Locate every blood parasite and identify its species.
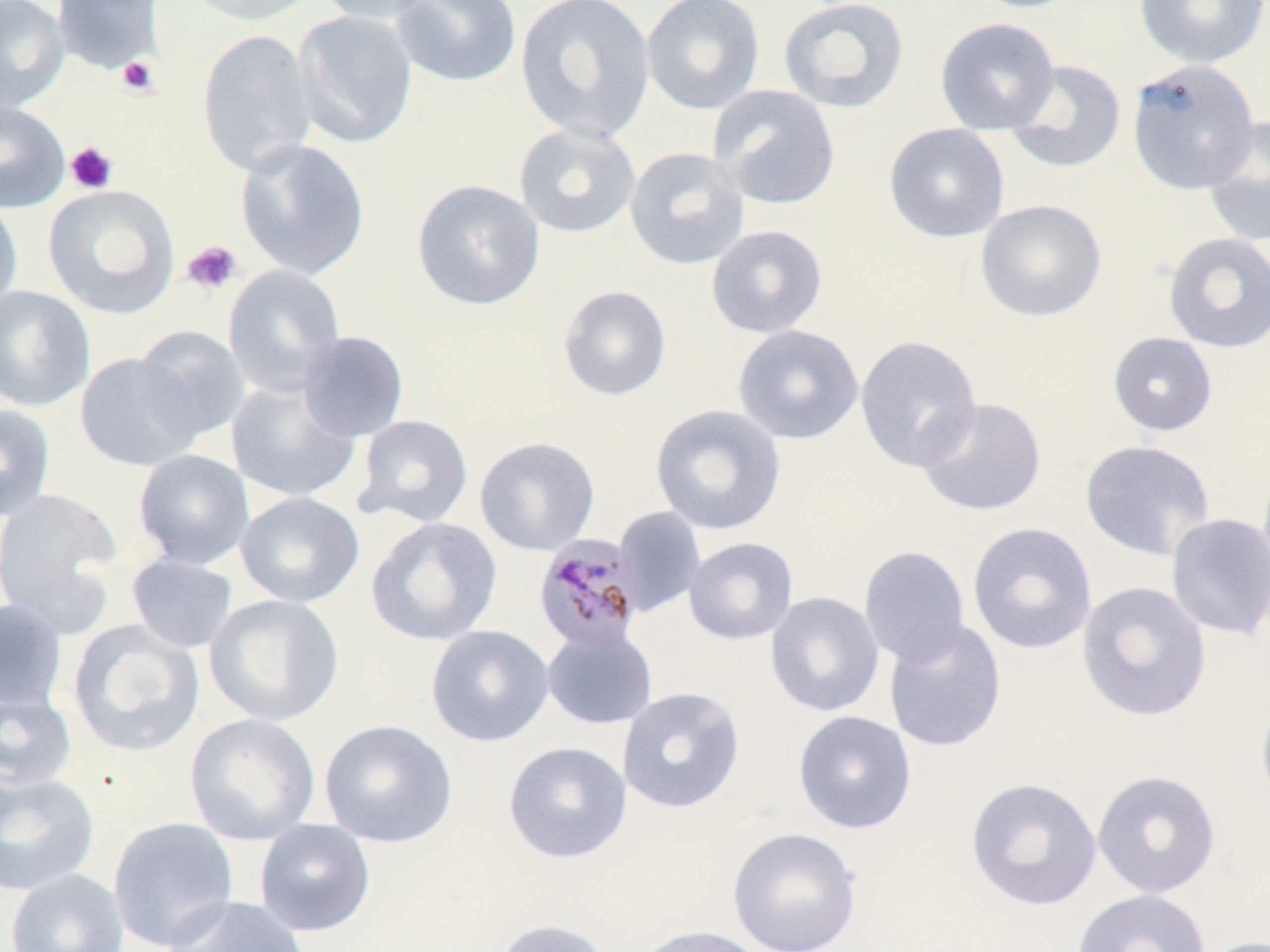

Approximate bounding boxes as (x1,y1)-(x2,y2) corner pairs in pixels.
Plasmodium malariae-infected red blood cells: (532,533)-(646,653).
No Plasmodium falciparum, Plasmodium ovale, Plasmodium vivax, Babesia divergens, or Trypanosoma brucei observed.

slide_level_diagnosis: Plasmodium malariae
modality: optical microscopy
platelet_locations: 'approximate bounding boxes as (x1,y1)-(x2,y2) corner pairs in pixels: (117,56)-(158,97), (65,142)-(118,194), (182,241)-(242,296)'
uninfected_red_blood_cell_locations: 'approximate bounding boxes as (x1,y1)-(x2,y2) corner pairs in pixels: (0,0)-(70,112), (51,0)-(162,74), (180,0)-(319,26), (316,0)-(441,25), (390,0)-(522,88), (515,0)-(657,144), (640,0)-(765,115), (1134,0)-(1269,69), (778,1)-(910,115), (292,10)-(418,149), (934,17)-(1060,135), (197,28)-(318,177), (1127,58)-(1262,195), (1003,59)-(1127,174), (708,84)-(841,210), (0,99)-(70,212), (1201,115)-(1270,247), (514,122)-(641,239), (883,123)-(1010,243), (234,138)-(371,281), (624,146)-(749,270), (411,178)-(545,311), (42,184)-(180,319), (0,197)-(23,315), (975,199)-(1107,322), (706,224)-(828,338), (1163,232)-(1270,353), (222,264)-(346,397), (0,285)-(96,412), (558,285)-(671,401), (732,324)-(864,444), (131,325)-(251,443), (296,330)-(410,442), (1108,331)-(1217,436), (854,334)-(983,472), (75,352)-(204,472), (226,378)-(361,503), (915,397)-(1047,517), (0,403)-(56,521), (650,404)-(786,535), (352,415)-(474,528), (474,437)-(600,556), (1079,439)-(1216,562), (132,449)-(255,570), (0,487)-(124,632), (235,491)-(365,608), (613,506)-(707,618), (1166,512)-(1270,641), (365,517)-(502,647), (967,522)-(1097,654), (683,537)-(798,645), (858,545)-(970,666), (126,554)-(239,653), (1077,581)-(1211,722), (765,591)-(885,717), (205,594)-(345,727), (0,599)-(69,714), (884,618)-(1006,753), (67,620)-(206,758), (425,625)-(554,747), (541,625)-(658,730), (1,685)-(78,791), (617,686)-(746,814), (1255,692)-(1270,809), (792,710)-(917,834), (184,713)-(321,846), (318,719)-(458,848), (503,741)-(632,864), (0,768)-(101,896), (1092,769)-(1222,899), (966,776)-(1102,911), (107,816)-(240,952), (253,819)-(376,937), (727,827)-(862,952), (6,868)-(130,952), (1072,889)-(1211,952), (164,896)-(311,952), (492,918)-(615,952), (632,924)-(774,952), (1198,935)-(1270,952)'
stain: May-Grünwald-Giemsa
magnification: 1000x
field_of_view: one of a larger specimen
preparation: thin blood smear
image_size: 1270×952 pixels